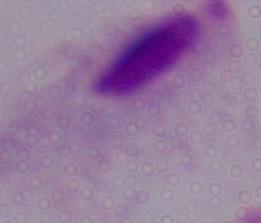

identification: trichomonad
magnification: 1000x
modality: micrograph